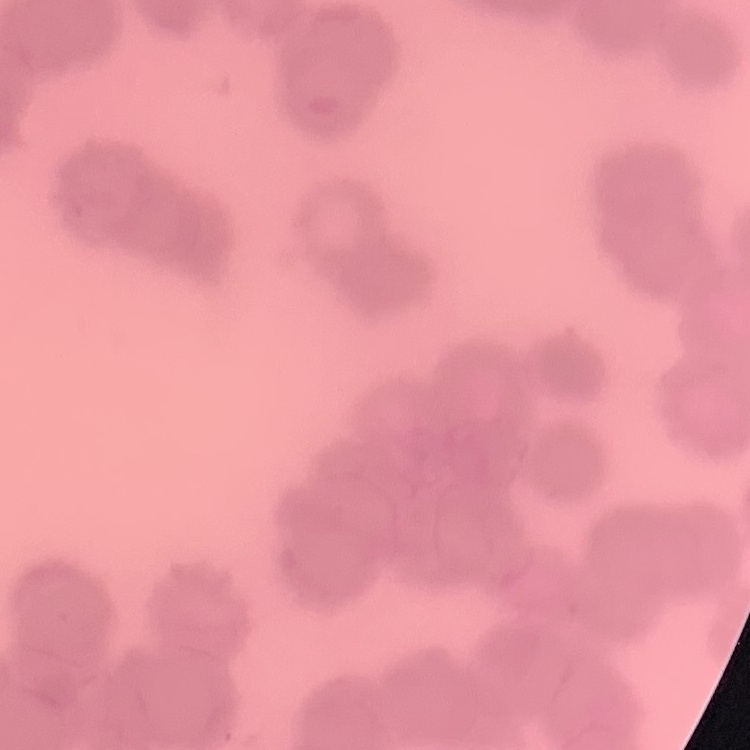

red_blood_cell_morphology: rouleaux formation
preparation: thin peripheral smear
image_type: square crop of a larger photomicrograph
stain: Field's or Giemsa